Classify this cell by malaria status.
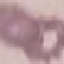
Uninfected.

image_type: automatically extracted cell patch, resized to 64 × 64 pixels
stain: Giemsa
preparation: thin blood smear
capture: smartphone through the microscope eyepiece